State the preparation type.
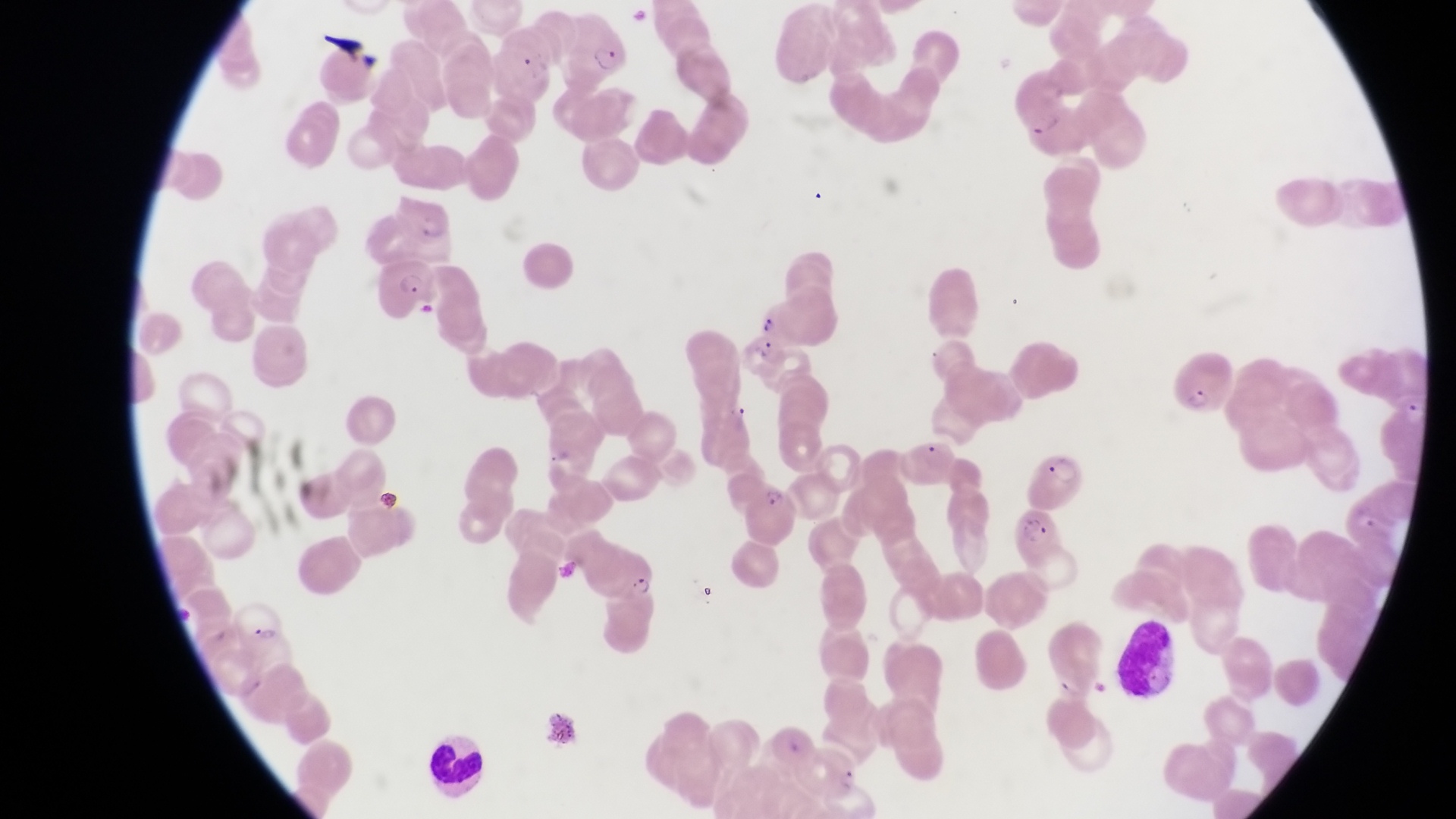

Thin blood smear.

Approximate bounding boxes as [left, top, right, bottom] in pixels. Artifact (platelet-like body, stain precipitate, or debris) locations: [377, 485, 407, 511], [697, 582, 723, 608]. Parasitised red blood cell locations: [558, 17, 636, 87], [377, 259, 438, 320], [748, 287, 821, 350], [1173, 350, 1233, 410], [1031, 451, 1086, 508], [745, 483, 797, 542], [1012, 512, 1067, 567], [587, 545, 660, 603], [230, 600, 283, 652]. Leukocyte locations: [1115, 617, 1178, 700], [428, 732, 488, 791]. One field of view. Photographed through the eyepiece of an Olympus CX-23 microscope with a smartphone camera. Image is 1456×819 pixels. Collected in Uganda. Magnification of 1000x.